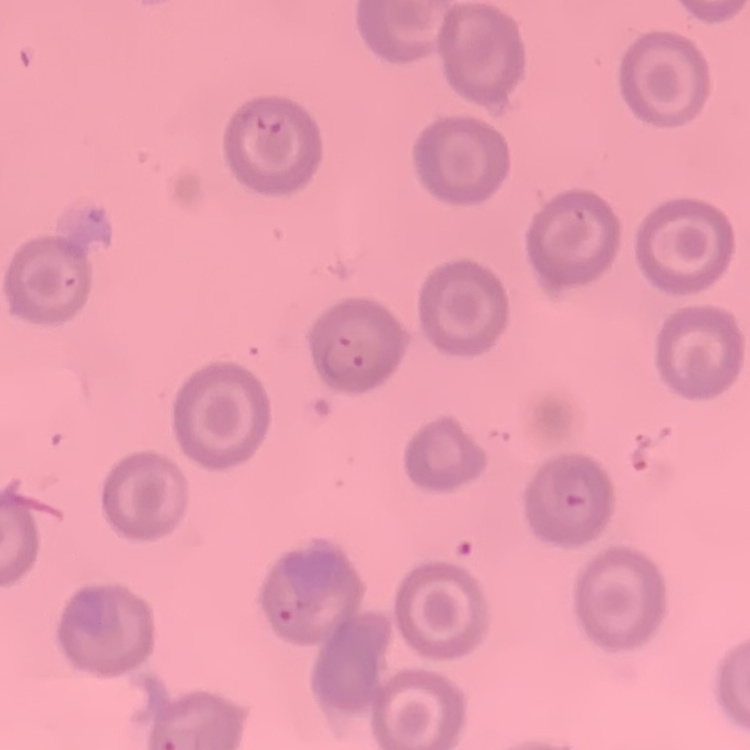

erythrocyte_morphology: no rouleaux formation
stain: Field's or Giemsa
preparation: thin peripheral smear
image_type: square crop of a larger photomicrograph